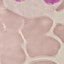

Summary:
  - Result: negative for malaria parasites
  - Image type: automatically extracted cell patch, resized to 64 × 64 pixels
  - Preparation: thin smear
  - Stain: Giemsa
  - Capture: smartphone camera at the microscope eyepiece